Report the malaria status of this cell.
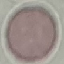
It is uninfected.

Summary:
  - Preparation: thin smear
  - Stain: Giemsa
  - Image type: automatically extracted cell patch, resized to 64 × 64 pixels
  - Capture: smartphone camera at the microscope eyepiece